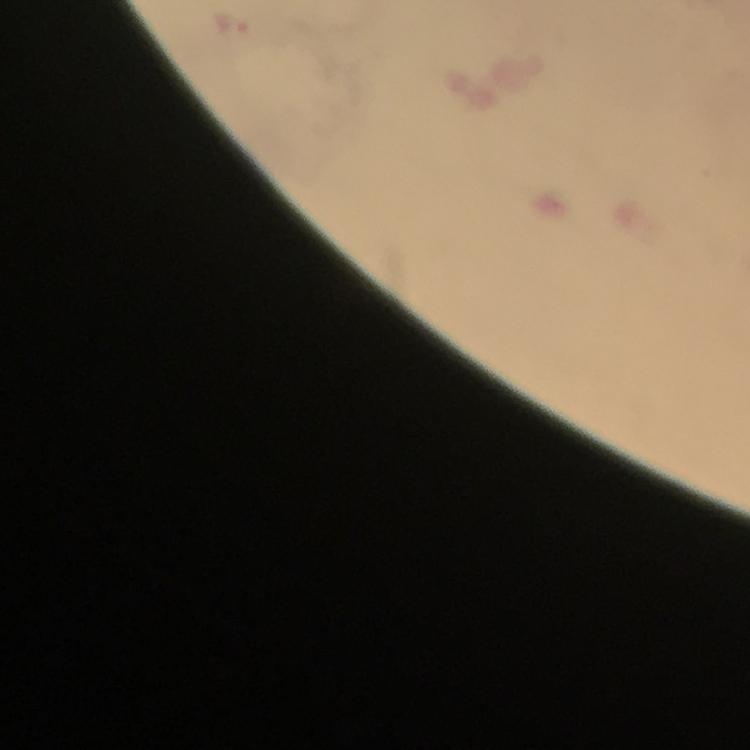
image size = 750×750 pixels
immersion oil = applied
capture = smartphone mounted on the microscope
malaria parasite locations = approximate object centers, in pixels from the top-left corner: (x=232, y=23)
preparation = thick smear
context = from a diagnostic examination for malaria
stain = Giemsa
magnification = 100x
cropped from = one field of view